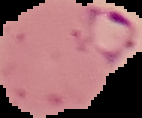 Image is 142×118 pixels. From a thin blood smear. Segmented cell region on a black background. Malaria status: parasitized.